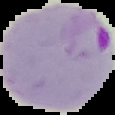 Malaria status: parasitized. Image is 115×115 pixels. Segmented cell region on a black background. From a thin blood film.